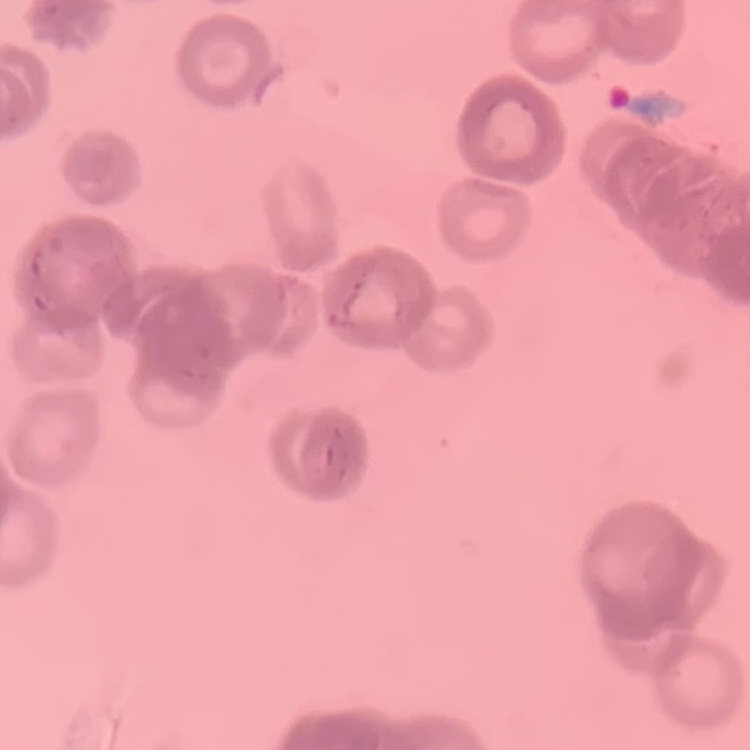

Summary:
  - Red blood cell morphology: rouleaux formation
  - Stain: Field's or Giemsa
  - Image type: square crop of a larger photomicrograph
  - Preparation: thin blood smear